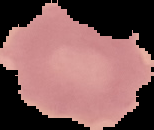

Cell region segmented out of the field of view; the surrounding area is masked to black. Image is 154×130 pixels. Malaria status: uninfected. From a thin blood film.